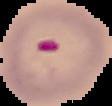 Image is 112×106 pixels. From a thin blood smear. Malaria status: parasitized. Segmented cell region on a black background.